Comment on the morphology of the red blood cells.
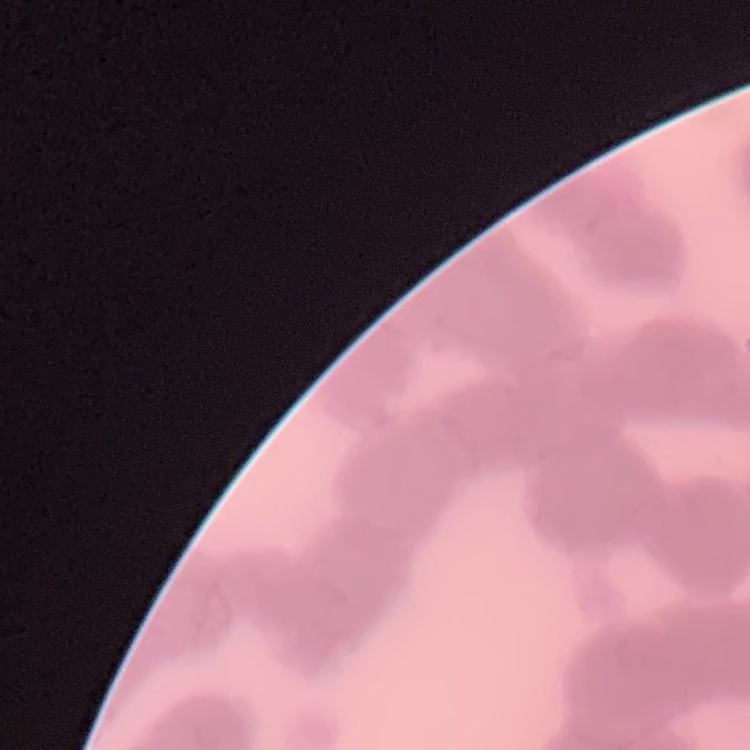
They show rouleaux formation.

preparation: thin peripheral smear
stain: Field's or Giemsa
image_type: square crop of a larger photomicrograph